Mark where white blood cells are.
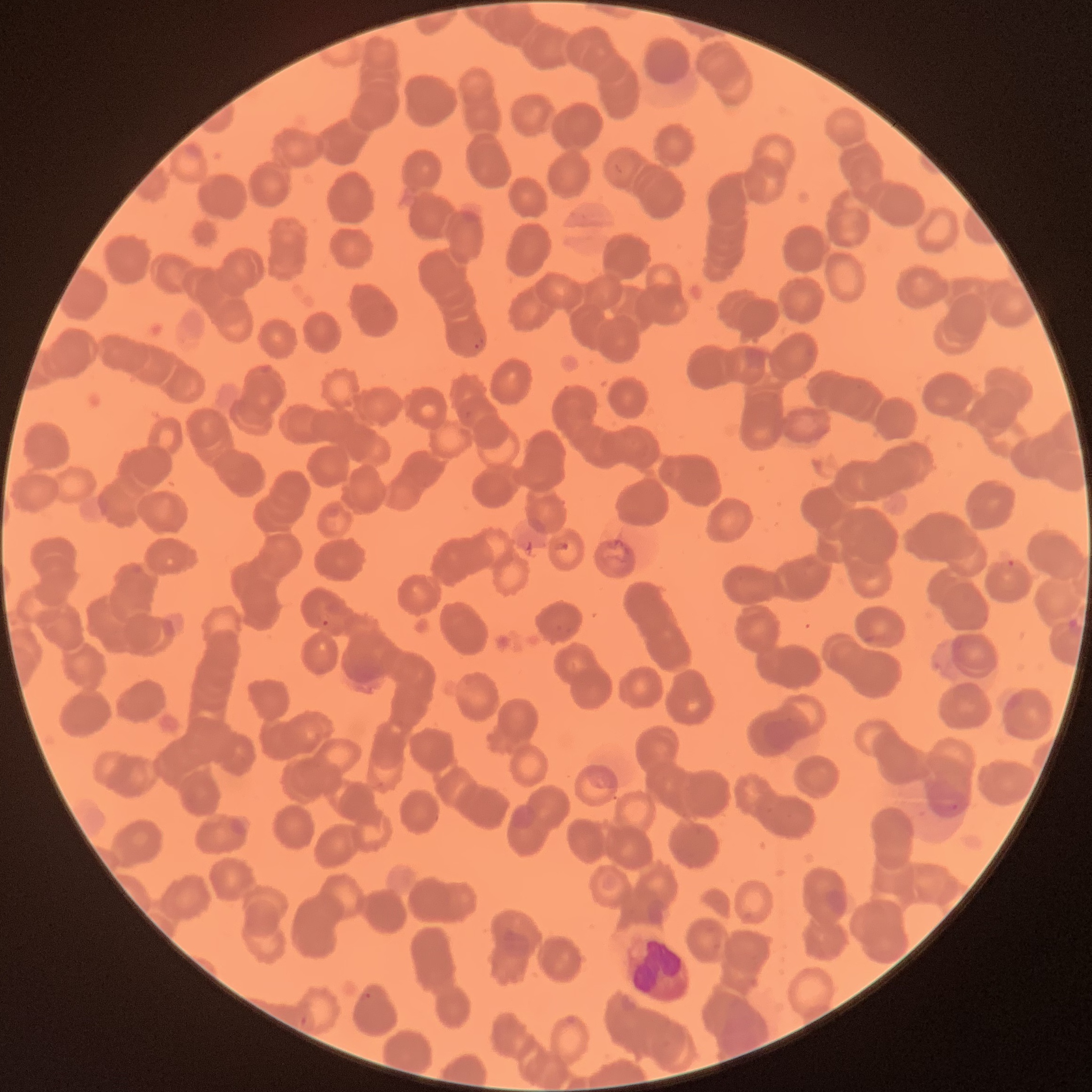
Approximate bounding boxes as (x1, y1, x2, y2) in pixels.
White blood cells: (625, 933, 689, 1001).

{
  "modality": "optical microscopy",
  "image_size": "1092×1092 pixels",
  "preparation": "thin blood film",
  "red_blood_cell_morphology": "rouleaux formation",
  "plasmodium_parasite_locations": "approximate bounding boxes as (x1, y1, x2, y2) in pixels: (474, 337, 482, 350), (464, 411, 474, 419), (314, 612, 331, 627), (556, 625, 572, 634), (925, 782, 967, 816), (357, 992, 371, 1002), (300, 1015, 306, 1029)"
}